Identify the preparation type.
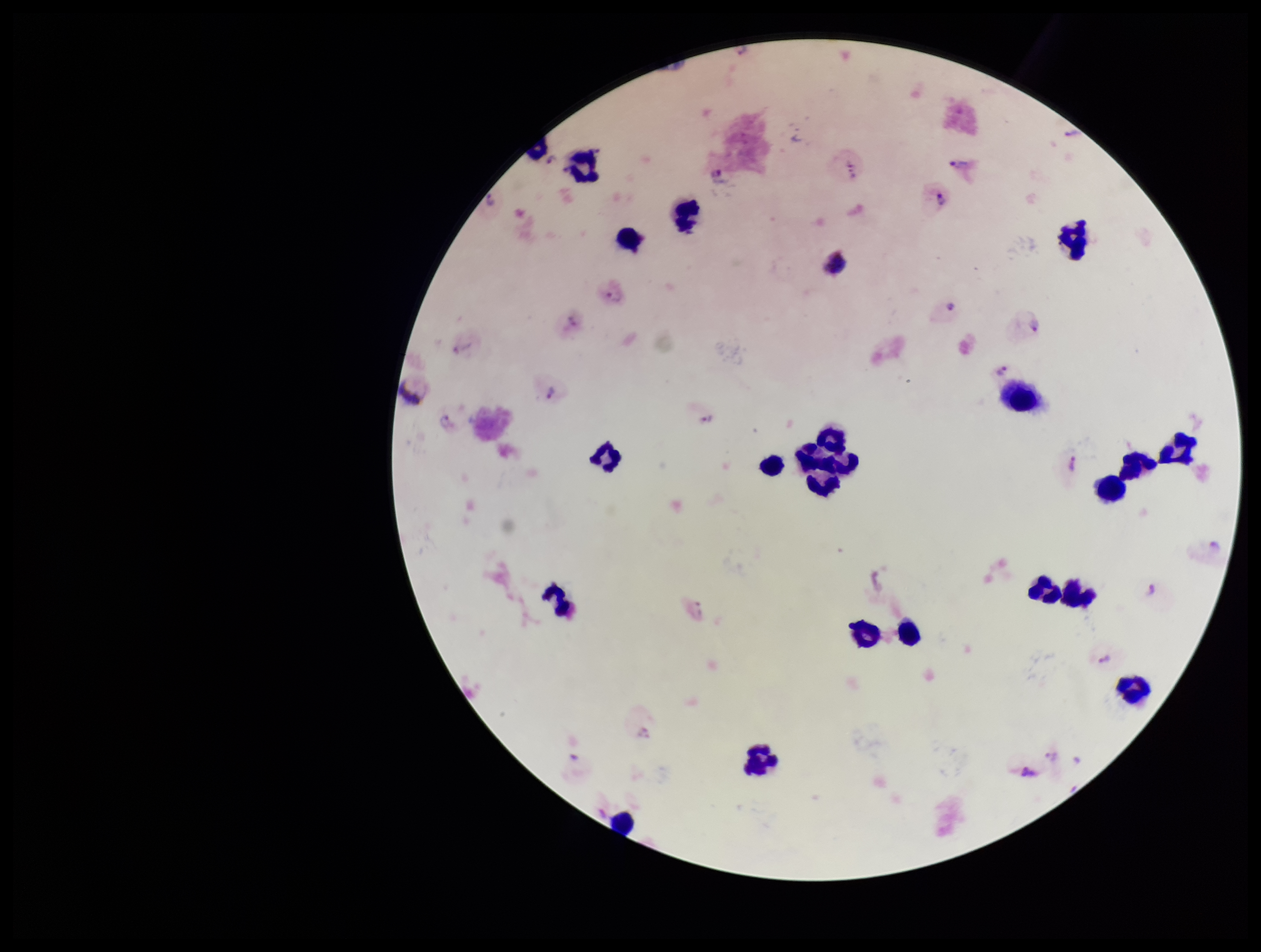

Thick.

Species reported for this patient: Plasmodium vivax. Parasite count: 23. One field from this slide. Patient malaria status: positive. Stained with Giemsa. Plasmodium parasites: seen. Leukocyte count: 23. Image is 1261×952 pixels. Smartphone photograph taken through the eyepiece of a microscope.